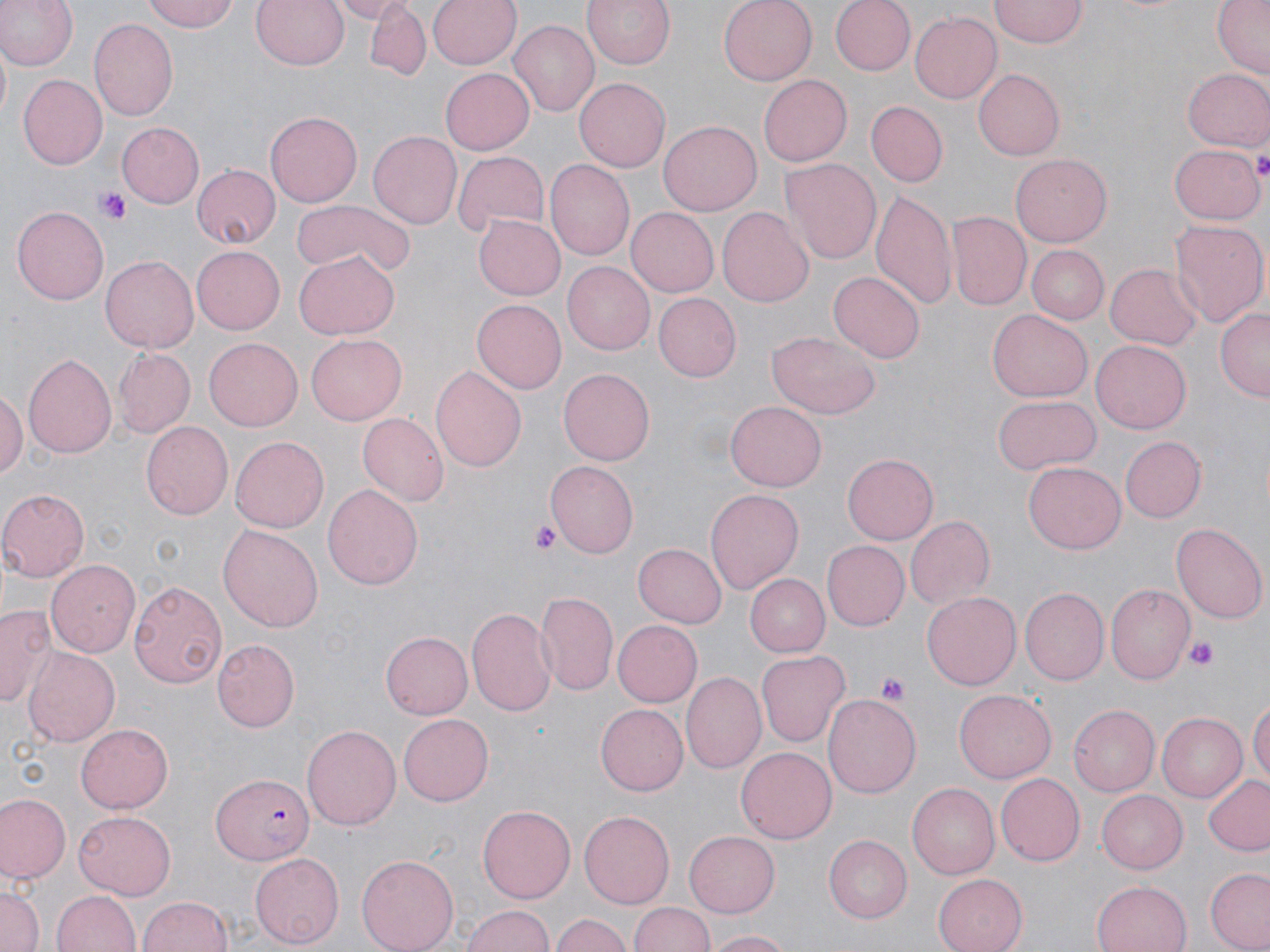

{
  "slide_level_diagnosis": "Plasmodium falciparum",
  "field_of_view": "single",
  "stain": "May-Grünwald-Giemsa",
  "magnification": "1000x",
  "plasmodium_falciparum_infected_red_blood_cell_locations": "approximate bounding boxes as named x1/y1/x2/y2 corners in pixels: (x1=209, y1=771, x2=317, y2=866)",
  "platelet_locations": "approximate bounding boxes as named x1/y1/x2/y2 corners in pixels: (x1=1254, y1=146, x2=1270, y2=179), (x1=97, y1=188, x2=133, y2=225), (x1=530, y1=522, x2=561, y2=556), (x1=1185, y1=637, x2=1221, y2=669), (x1=876, y1=672, x2=911, y2=704)",
  "modality": "light microscopy",
  "image_size": "1270×952 pixels",
  "preparation": "thin blood smear",
  "uninfected_red_blood_cell_locations": "approximate bounding boxes as named x1/y1/x2/y2 corners in pixels: (x1=0, y1=0, x2=77, y2=72), (x1=141, y1=0, x2=239, y2=33), (x1=252, y1=0, x2=348, y2=71), (x1=333, y1=0, x2=410, y2=22), (x1=428, y1=0, x2=521, y2=70), (x1=581, y1=0, x2=677, y2=69), (x1=718, y1=0, x2=817, y2=85), (x1=831, y1=0, x2=912, y2=75), (x1=992, y1=0, x2=1088, y2=46), (x1=1210, y1=0, x2=1270, y2=80), (x1=365, y1=4, x2=430, y2=80), (x1=911, y1=12, x2=1001, y2=104), (x1=89, y1=18, x2=180, y2=123), (x1=508, y1=20, x2=600, y2=117), (x1=440, y1=67, x2=533, y2=153), (x1=1183, y1=67, x2=1270, y2=152), (x1=974, y1=70, x2=1065, y2=160), (x1=19, y1=74, x2=108, y2=169), (x1=757, y1=75, x2=850, y2=166), (x1=574, y1=77, x2=671, y2=173), (x1=866, y1=100, x2=949, y2=187), (x1=265, y1=111, x2=360, y2=207), (x1=658, y1=120, x2=761, y2=216), (x1=118, y1=124, x2=204, y2=207), (x1=370, y1=130, x2=462, y2=231), (x1=1170, y1=144, x2=1263, y2=223), (x1=451, y1=148, x2=550, y2=237), (x1=1011, y1=154, x2=1112, y2=247), (x1=781, y1=157, x2=882, y2=265), (x1=545, y1=159, x2=634, y2=260), (x1=192, y1=165, x2=280, y2=246), (x1=871, y1=191, x2=956, y2=313), (x1=292, y1=199, x2=414, y2=277), (x1=11, y1=206, x2=110, y2=304), (x1=627, y1=208, x2=718, y2=298), (x1=718, y1=208, x2=814, y2=306), (x1=949, y1=211, x2=1031, y2=310), (x1=474, y1=215, x2=564, y2=300), (x1=1167, y1=219, x2=1267, y2=328), (x1=193, y1=244, x2=287, y2=333), (x1=1027, y1=245, x2=1109, y2=324), (x1=293, y1=252, x2=398, y2=338), (x1=100, y1=254, x2=199, y2=353), (x1=1107, y1=262, x2=1202, y2=349), (x1=562, y1=263, x2=654, y2=355), (x1=828, y1=272, x2=925, y2=363), (x1=654, y1=293, x2=741, y2=380), (x1=471, y1=299, x2=564, y2=394), (x1=1216, y1=307, x2=1269, y2=403), (x1=988, y1=310, x2=1091, y2=401), (x1=766, y1=332, x2=882, y2=418), (x1=306, y1=334, x2=405, y2=424), (x1=203, y1=336, x2=303, y2=430), (x1=1091, y1=340, x2=1191, y2=432), (x1=111, y1=347, x2=196, y2=439), (x1=23, y1=353, x2=116, y2=461), (x1=431, y1=364, x2=526, y2=471), (x1=558, y1=368, x2=655, y2=465), (x1=0, y1=386, x2=25, y2=488), (x1=992, y1=395, x2=1100, y2=474), (x1=726, y1=402, x2=825, y2=492), (x1=357, y1=412, x2=447, y2=505), (x1=140, y1=422, x2=234, y2=521), (x1=230, y1=436, x2=328, y2=533), (x1=1121, y1=438, x2=1207, y2=522), (x1=842, y1=451, x2=938, y2=544), (x1=547, y1=461, x2=639, y2=557), (x1=1024, y1=462, x2=1125, y2=554), (x1=324, y1=484, x2=422, y2=591), (x1=706, y1=486, x2=803, y2=592), (x1=0, y1=489, x2=89, y2=580), (x1=905, y1=515, x2=997, y2=611), (x1=1171, y1=522, x2=1266, y2=623), (x1=217, y1=523, x2=324, y2=633), (x1=821, y1=539, x2=908, y2=629), (x1=632, y1=542, x2=726, y2=627), (x1=47, y1=558, x2=143, y2=657), (x1=743, y1=573, x2=829, y2=657), (x1=130, y1=581, x2=228, y2=688), (x1=1105, y1=584, x2=1194, y2=683), (x1=1021, y1=588, x2=1109, y2=684), (x1=535, y1=590, x2=620, y2=698), (x1=922, y1=591, x2=1022, y2=690), (x1=1, y1=603, x2=58, y2=709), (x1=468, y1=607, x2=556, y2=719), (x1=613, y1=619, x2=701, y2=706), (x1=381, y1=629, x2=473, y2=719), (x1=214, y1=639, x2=299, y2=731), (x1=22, y1=647, x2=119, y2=747), (x1=757, y1=651, x2=849, y2=746), (x1=681, y1=673, x2=765, y2=777), (x1=955, y1=690, x2=1056, y2=782), (x1=823, y1=695, x2=921, y2=796), (x1=1250, y1=698, x2=1269, y2=789), (x1=597, y1=704, x2=688, y2=795), (x1=1069, y1=706, x2=1159, y2=796), (x1=1155, y1=713, x2=1248, y2=803), (x1=398, y1=714, x2=494, y2=805), (x1=75, y1=722, x2=175, y2=813), (x1=303, y1=723, x2=400, y2=831), (x1=737, y1=745, x2=836, y2=841), (x1=994, y1=772, x2=1084, y2=866), (x1=1201, y1=774, x2=1270, y2=855), (x1=909, y1=782, x2=1003, y2=879), (x1=1098, y1=790, x2=1190, y2=873), (x1=1, y1=794, x2=70, y2=882), (x1=476, y1=804, x2=575, y2=903), (x1=580, y1=811, x2=674, y2=907), (x1=73, y1=812, x2=177, y2=898), (x1=685, y1=832, x2=780, y2=916), (x1=822, y1=836, x2=910, y2=923), (x1=249, y1=853, x2=342, y2=948), (x1=356, y1=855, x2=459, y2=952), (x1=1205, y1=869, x2=1270, y2=952), (x1=933, y1=874, x2=1026, y2=952), (x1=1092, y1=880, x2=1193, y2=952), (x1=0, y1=881, x2=42, y2=952), (x1=54, y1=890, x2=140, y2=952), (x1=137, y1=894, x2=233, y2=952), (x1=630, y1=901, x2=716, y2=952), (x1=460, y1=905, x2=556, y2=952), (x1=551, y1=912, x2=634, y2=952), (x1=706, y1=929, x2=795, y2=952)"
}